Report the malaria status of this cell.
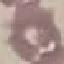

Uninfected.

Summary:
  - Capture: smartphone camera at the microscope eyepiece
  - Preparation: thin blood smear
  - Stain: Giemsa
  - Image type: automatically extracted cell patch, resized to 64 × 64 pixels